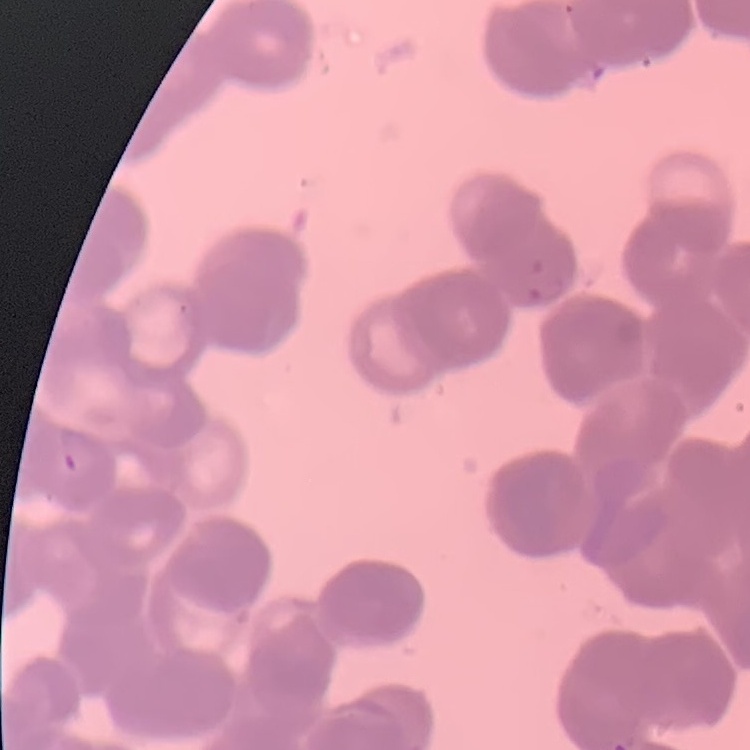

The erythrocytes show rouleaux formation. Square crop of a larger photomicrograph. Thin blood film. Stained with either Field's or Giemsa.